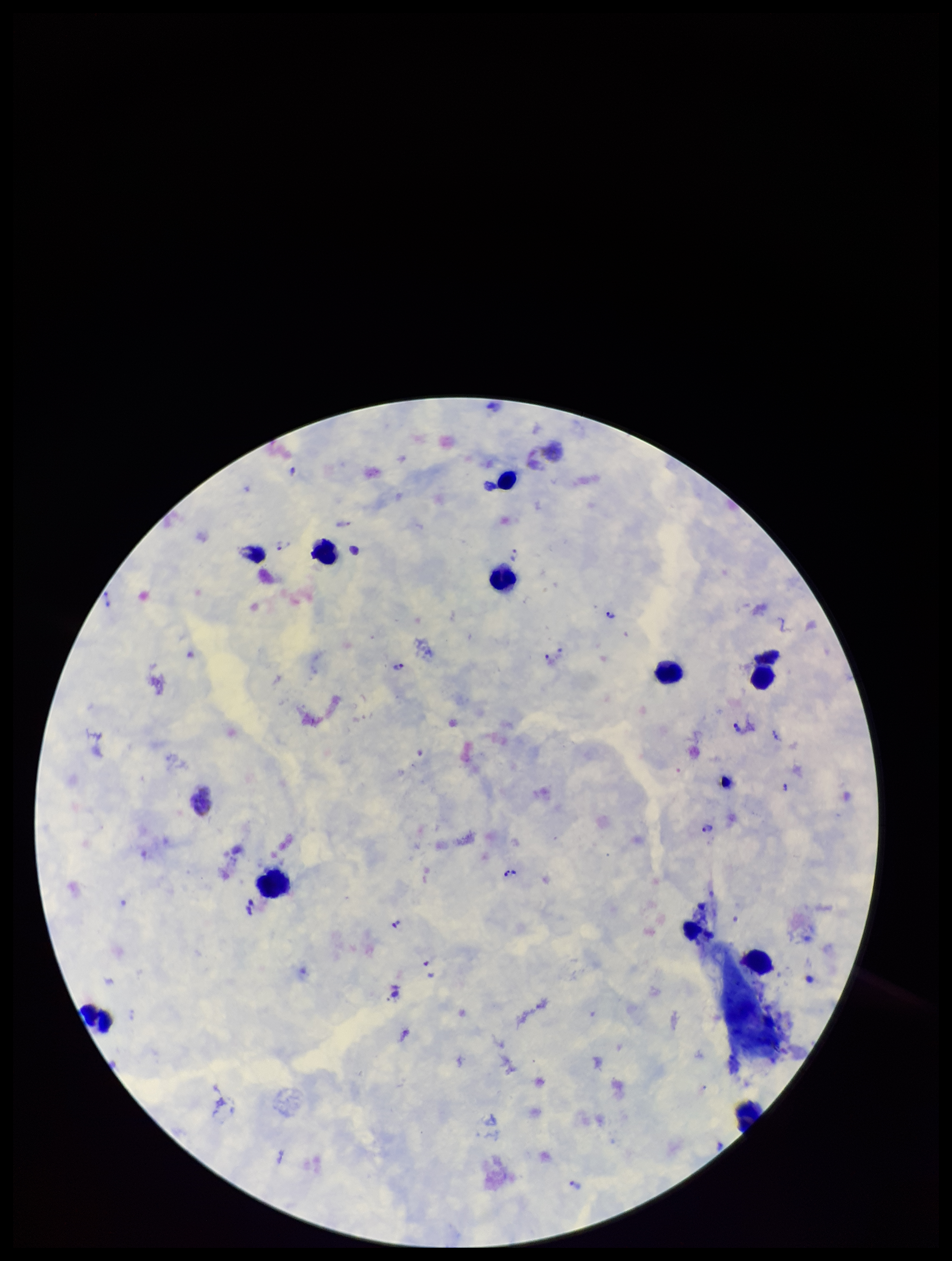

parasite count = 16
image size = 952×1261 pixels
patient malaria status = infected
Plasmodium parasites = identified
capture = smartphone photograph through the microscope eyepiece
species reported for this patient = Plasmodium vivax
preparation = thick
leukocyte count = 9
field of view = single
stain = Giemsa